State which parasite is depicted.
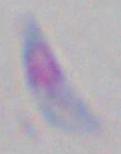
Toxoplasma gondii.

Photomicrograph. 1000x magnification.